Report the malaria status of this cell.
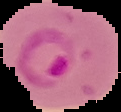

Parasitized.

From a thin blood film. The area outside the segmented cell region is set to black. Image is 121×112 pixels.